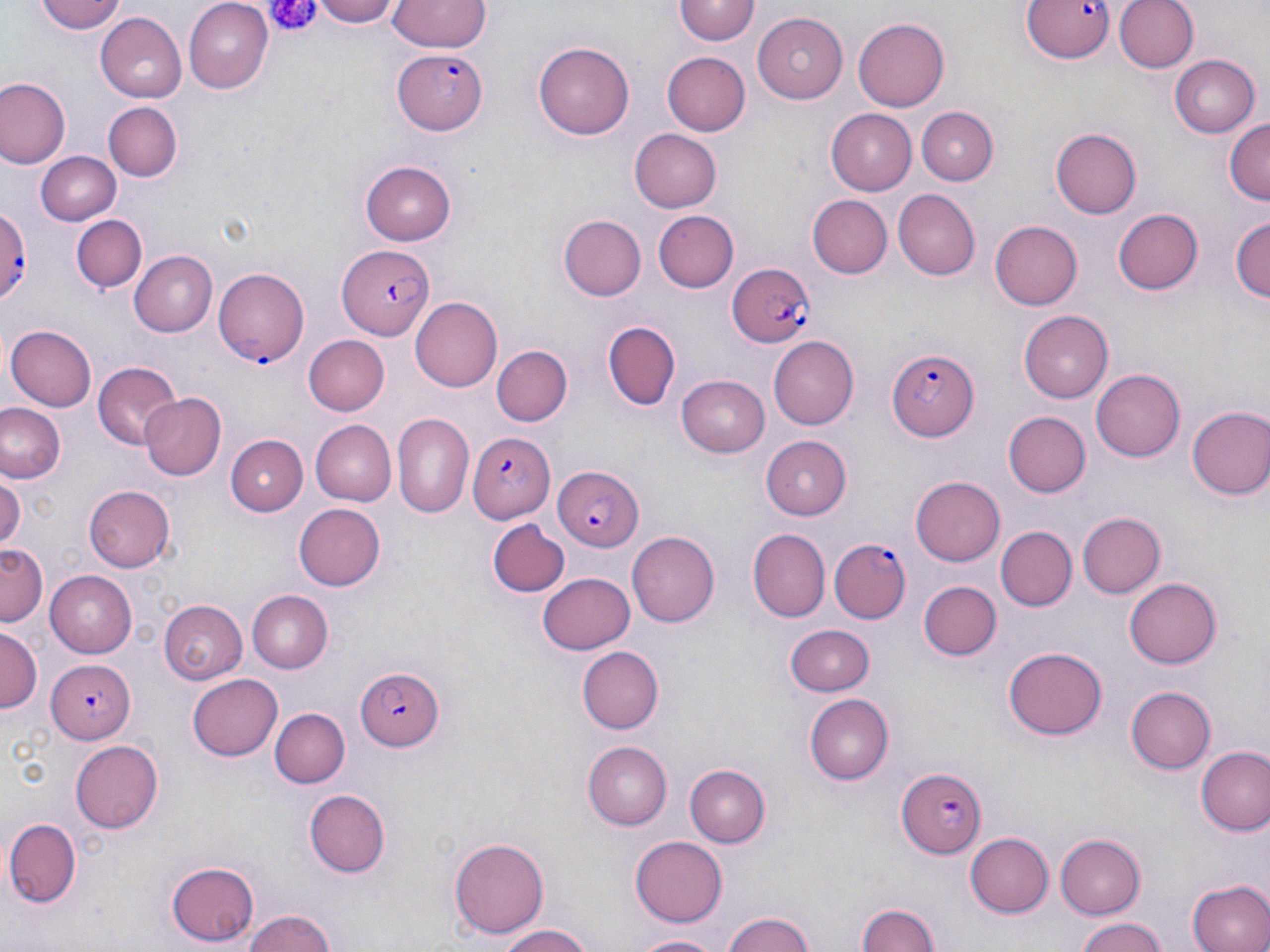 Approximate bounding boxes as named x1/y1/x2/y2 corners in pixels. Platelet locations: (x1=261, y1=1, x2=319, y2=41). Uninfected red blood cell locations: (x1=35, y1=0, x2=127, y2=34), (x1=183, y1=0, x2=273, y2=90), (x1=313, y1=0, x2=403, y2=26), (x1=387, y1=0, x2=489, y2=52), (x1=1113, y1=0, x2=1195, y2=73), (x1=675, y1=1, x2=759, y2=46), (x1=97, y1=12, x2=187, y2=102), (x1=753, y1=12, x2=847, y2=103), (x1=854, y1=19, x2=950, y2=112), (x1=534, y1=41, x2=635, y2=139), (x1=661, y1=51, x2=749, y2=135), (x1=1168, y1=54, x2=1259, y2=137), (x1=0, y1=79, x2=69, y2=168), (x1=104, y1=102, x2=181, y2=180), (x1=917, y1=106, x2=997, y2=184), (x1=826, y1=108, x2=916, y2=194), (x1=1224, y1=118, x2=1270, y2=206), (x1=628, y1=128, x2=721, y2=213), (x1=1051, y1=129, x2=1141, y2=217), (x1=36, y1=151, x2=122, y2=227), (x1=360, y1=161, x2=457, y2=245), (x1=893, y1=189, x2=981, y2=279), (x1=806, y1=193, x2=891, y2=276), (x1=1113, y1=208, x2=1204, y2=295), (x1=653, y1=209, x2=740, y2=293), (x1=72, y1=215, x2=147, y2=295), (x1=559, y1=216, x2=645, y2=301), (x1=1230, y1=217, x2=1268, y2=307), (x1=990, y1=220, x2=1082, y2=310), (x1=131, y1=250, x2=217, y2=338), (x1=409, y1=297, x2=501, y2=392), (x1=1022, y1=309, x2=1116, y2=402), (x1=601, y1=320, x2=680, y2=410), (x1=5, y1=324, x2=97, y2=411), (x1=300, y1=334, x2=389, y2=416), (x1=770, y1=337, x2=860, y2=428), (x1=492, y1=346, x2=573, y2=426), (x1=93, y1=362, x2=184, y2=451), (x1=1090, y1=368, x2=1185, y2=461), (x1=677, y1=374, x2=771, y2=457), (x1=138, y1=392, x2=226, y2=481), (x1=0, y1=403, x2=66, y2=484), (x1=1187, y1=405, x2=1270, y2=501), (x1=1004, y1=412, x2=1092, y2=497), (x1=392, y1=413, x2=473, y2=519), (x1=312, y1=420, x2=395, y2=504), (x1=226, y1=434, x2=308, y2=516), (x1=762, y1=434, x2=853, y2=520), (x1=0, y1=474, x2=24, y2=551), (x1=911, y1=476, x2=1005, y2=566), (x1=84, y1=486, x2=175, y2=573), (x1=295, y1=504, x2=386, y2=590), (x1=1076, y1=512, x2=1163, y2=598), (x1=489, y1=522, x2=570, y2=598), (x1=996, y1=526, x2=1077, y2=611), (x1=747, y1=528, x2=830, y2=621), (x1=628, y1=530, x2=720, y2=626), (x1=1, y1=543, x2=45, y2=627), (x1=44, y1=571, x2=138, y2=656), (x1=538, y1=572, x2=633, y2=654), (x1=1124, y1=578, x2=1222, y2=668), (x1=918, y1=580, x2=1000, y2=660), (x1=247, y1=590, x2=333, y2=672), (x1=159, y1=599, x2=247, y2=682), (x1=786, y1=622, x2=876, y2=695), (x1=1, y1=628, x2=40, y2=711), (x1=1003, y1=645, x2=1107, y2=740), (x1=579, y1=646, x2=663, y2=734), (x1=188, y1=675, x2=283, y2=762), (x1=1127, y1=684, x2=1217, y2=775), (x1=804, y1=694, x2=894, y2=785), (x1=270, y1=708, x2=349, y2=787), (x1=70, y1=739, x2=163, y2=833), (x1=582, y1=741, x2=671, y2=829), (x1=1194, y1=746, x2=1269, y2=836), (x1=684, y1=763, x2=771, y2=848), (x1=304, y1=789, x2=389, y2=878), (x1=3, y1=820, x2=83, y2=906), (x1=964, y1=833, x2=1053, y2=916), (x1=1057, y1=833, x2=1147, y2=918), (x1=450, y1=835, x2=548, y2=936), (x1=630, y1=836, x2=726, y2=926), (x1=166, y1=861, x2=258, y2=947), (x1=1186, y1=879, x2=1270, y2=952), (x1=854, y1=902, x2=944, y2=952), (x1=238, y1=907, x2=341, y2=952), (x1=720, y1=912, x2=821, y2=952), (x1=1073, y1=917, x2=1169, y2=952), (x1=494, y1=922, x2=598, y2=952), (x1=632, y1=933, x2=725, y2=951). Plasmodium falciparum-infected red blood cell locations: (x1=1020, y1=0, x2=1116, y2=65), (x1=393, y1=48, x2=488, y2=135), (x1=0, y1=206, x2=34, y2=300), (x1=339, y1=247, x2=434, y2=338), (x1=725, y1=264, x2=817, y2=349), (x1=215, y1=268, x2=309, y2=366), (x1=885, y1=349, x2=976, y2=440), (x1=470, y1=430, x2=556, y2=525), (x1=551, y1=465, x2=643, y2=551), (x1=828, y1=537, x2=909, y2=623), (x1=44, y1=658, x2=134, y2=742), (x1=355, y1=668, x2=444, y2=751), (x1=896, y1=767, x2=989, y2=856). Slide-level diagnosis: Plasmodium falciparum. Image is 1270×952 pixels. 1000x magnification. Optical microscopy. One field of a larger specimen. Thin blood film. May-Grünwald-Giemsa stain.